Report the malaria status of this cell.
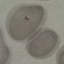
Parasitized.

Photographed with a smartphone camera at the microscope eyepiece. Thin blood film. Giemsa stain. Cell patch, automatically extracted from a larger field of view and resized to 64 × 64 pixels.